Report the malaria status.
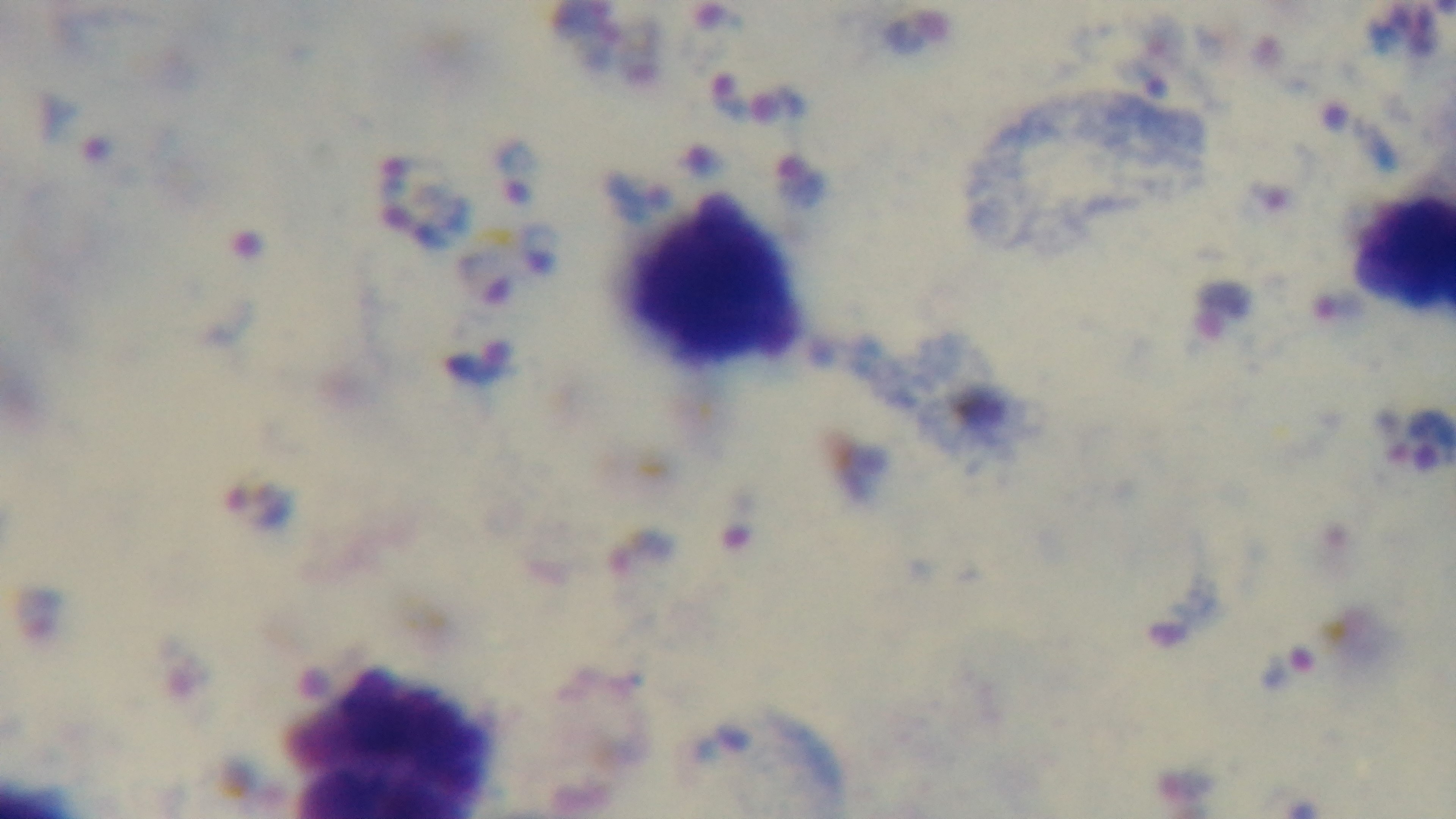

Infected.

Summary:
  - Objective: 100x oil immersion
  - Capture: mounted 4K digital camera
  - Modality: light microscopy
  - Preparation: thick
  - Stain: Giemsa
  - Field of view: one from the slide